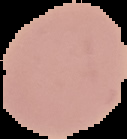

image size = 127×139 pixels
malaria status = uninfected
image type = segmented cell region with the area outside set to black
preparation = thin blood film